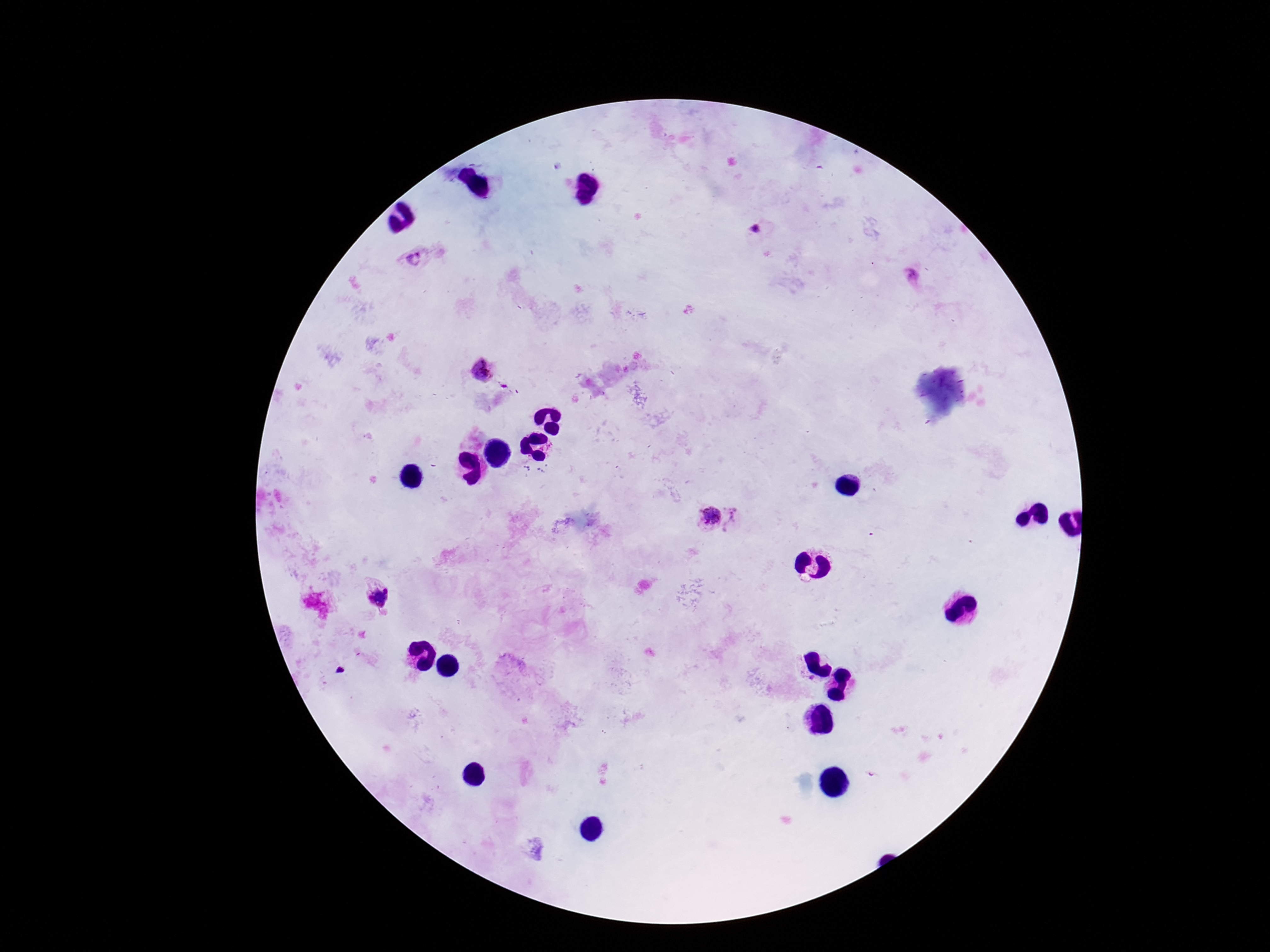

magnification = 100x
preparation = thick blood smear
Plasmodium parasite locations = approximate centers as {x, y} in pixels: {757, 230}, {414, 258}, {910, 274}, {482, 370}, {707, 515}, {741, 519}, {377, 597}
patient malaria status = positive
stain = Giemsa
field of view = single
image size = 1270×952 pixels
capture = smartphone camera through the microscope eyepiece